Classify the preparation.
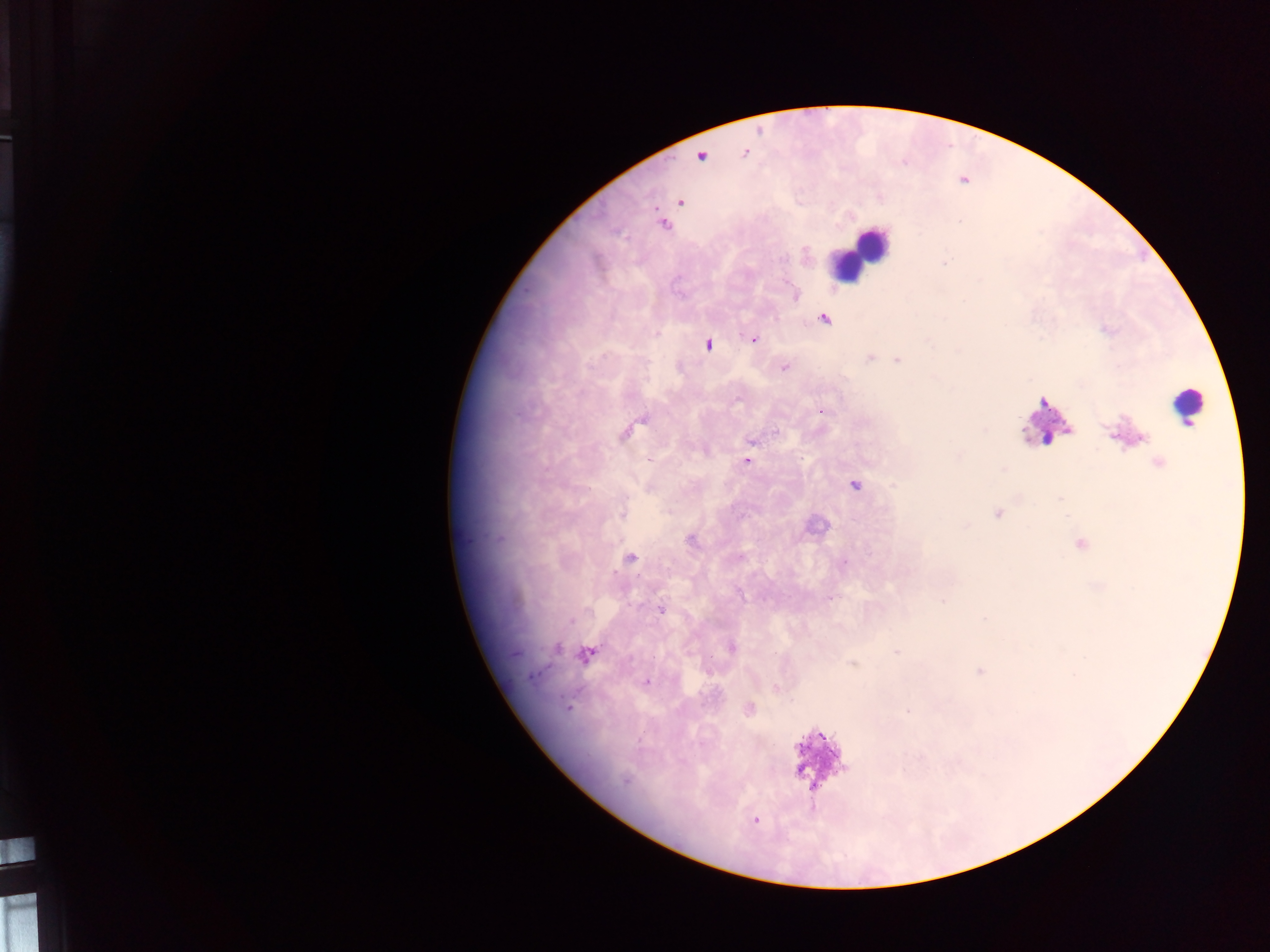
Thick blood smear.

Approximate centers as {x, y} in pixels. Plasmodium parasite locations: {701, 156}, {680, 202}, {824, 320}, {656, 334}, {753, 339}, {708, 344}, {870, 358}, {897, 360}, {784, 368}, {821, 411}, {626, 433}, {751, 441}, {747, 462}, {1158, 463}, {855, 485}, {622, 512}, {998, 513}, {691, 541}, {631, 559}, {844, 563}, {831, 598}, {943, 601}, {661, 610}, {571, 621}, {557, 648}, {731, 648}, {897, 651}, {587, 655}, {853, 664}, {980, 671}, {533, 675}, {646, 681}, {775, 688}, {568, 707}, {749, 708}, {907, 711}, {625, 780}, {755, 820}. Leukocyte locations: {858, 254}, {1185, 405}, {1046, 417}, {813, 527}, {811, 756}. Mobile-phone photograph taken through the microscope. Single field of view. Collected in Ghana. Image is 1270×952 pixels.